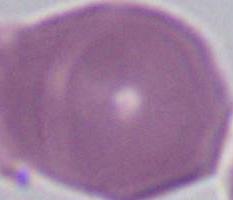

Summary:
  - Modality: photomicrograph
  - Identification: red blood cell
  - Magnification: 1000x